Locate malaria parasites and leukocytes.
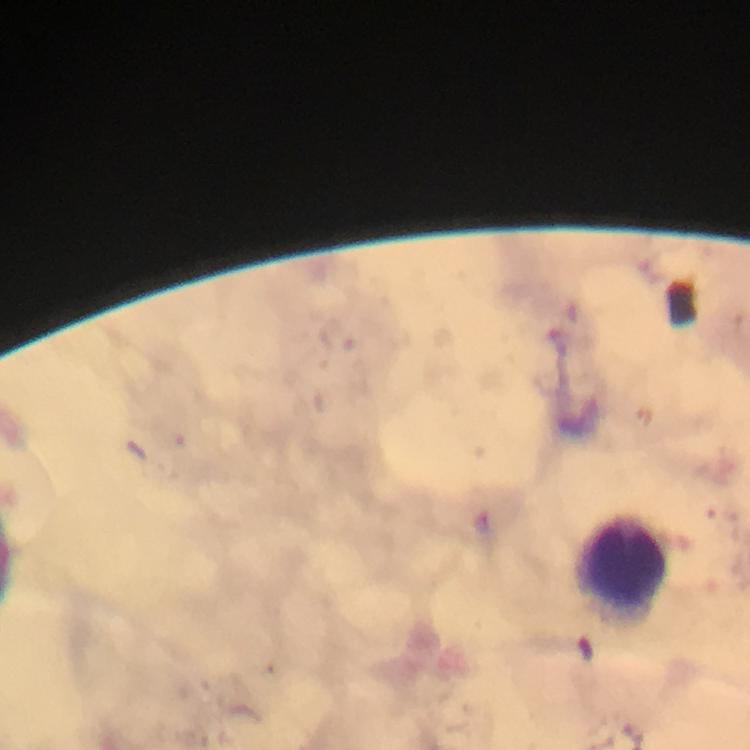
No malaria parasites detected.
Approximate object centers, in pixels from the top-left corner.
Leukocytes: (x=623, y=559).

Smartphone photograph taken through a microscope. Giemsa-stained preparation. Immersion oil was used. Image is 750×750 pixels. Thick blood smear. A crop from one field of view. From a malaria diagnostic workup. At 100x magnification.